Identify the parasite.
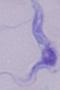

A trypanosome.

magnification = 1000x
modality = micrograph